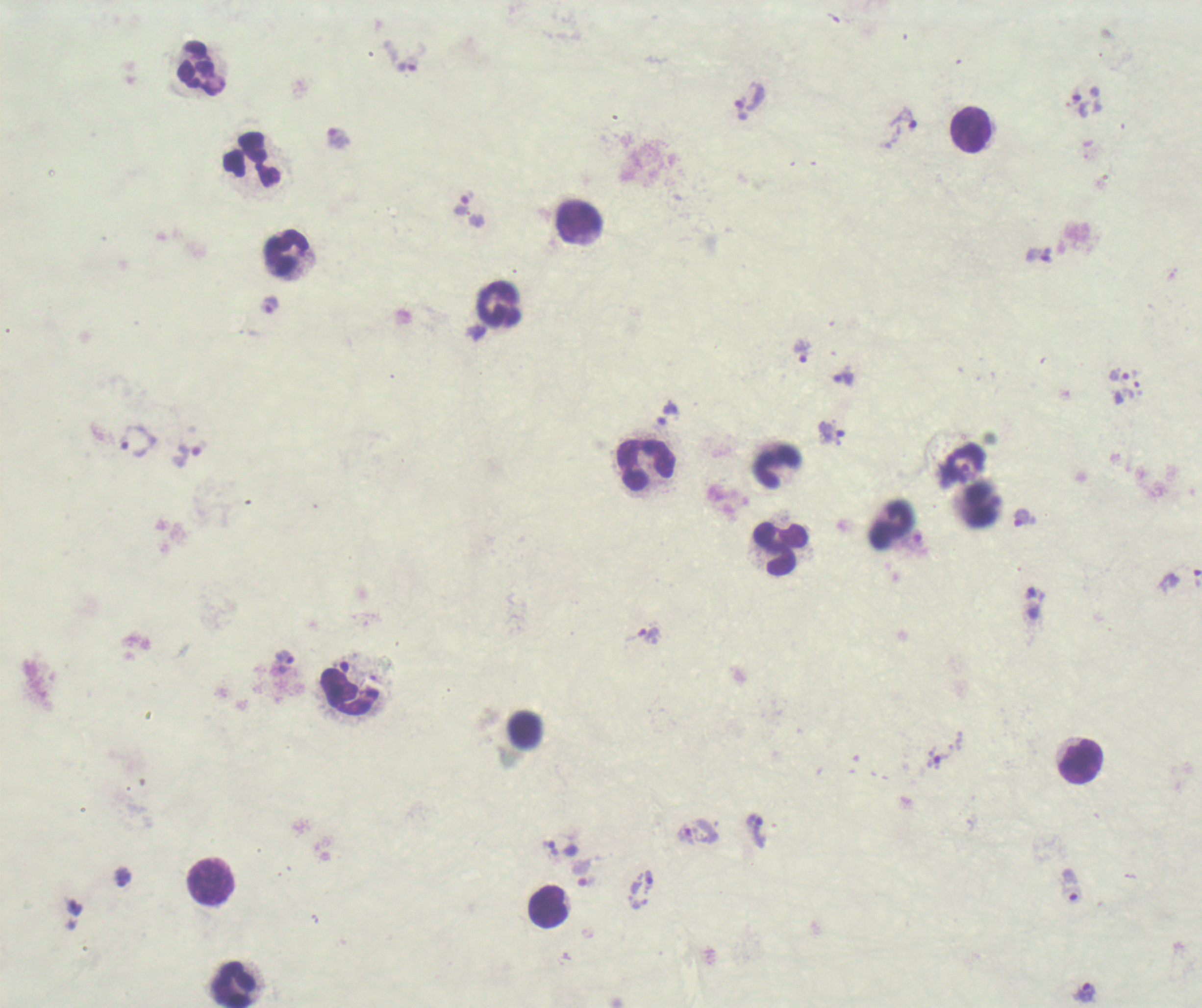

coordinate format = approximate centers as [x, y] in pixels
leukocyte locations = [200, 66], [970, 130], [252, 158], [579, 218], [287, 251], [499, 303], [645, 464], [776, 466], [890, 524], [779, 548], [349, 692], [525, 729], [1080, 762], [211, 882], [547, 907], [234, 983]
trophozoite locations = [406, 67], [740, 109], [903, 119], [339, 138], [463, 203], [270, 304], [802, 351], [1118, 374], [844, 378], [831, 433], [138, 440], [189, 453], [1021, 517], [1196, 578], [649, 635], [284, 657], [936, 760], [755, 821], [550, 848], [587, 881], [640, 890], [1083, 993]
coloration quality = bad
result = malaria parasites detected
image size = 1202×1008 pixels
magnification = 100x
context = previously used in an actual diagnosis
background quality = poor
stain = Romanowsky
field of view = one from this slide
preparation = thick blood smear